Comment on the morphology of the red blood cells.
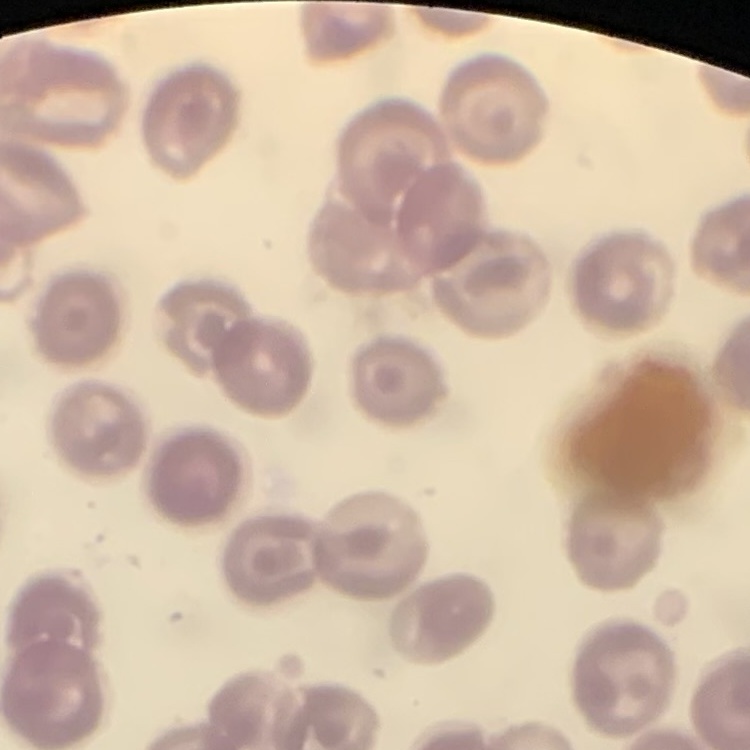
No rouleaux formation.

{
  "stain": "Field's or Giemsa",
  "preparation": "thin blood smear",
  "image_type": "square crop of a larger photomicrograph"
}